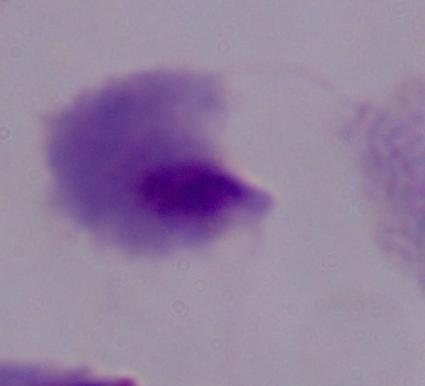 A trichomonad is seen. 1000x magnification. Micrograph.